Locate every blood parasite and identify its species.
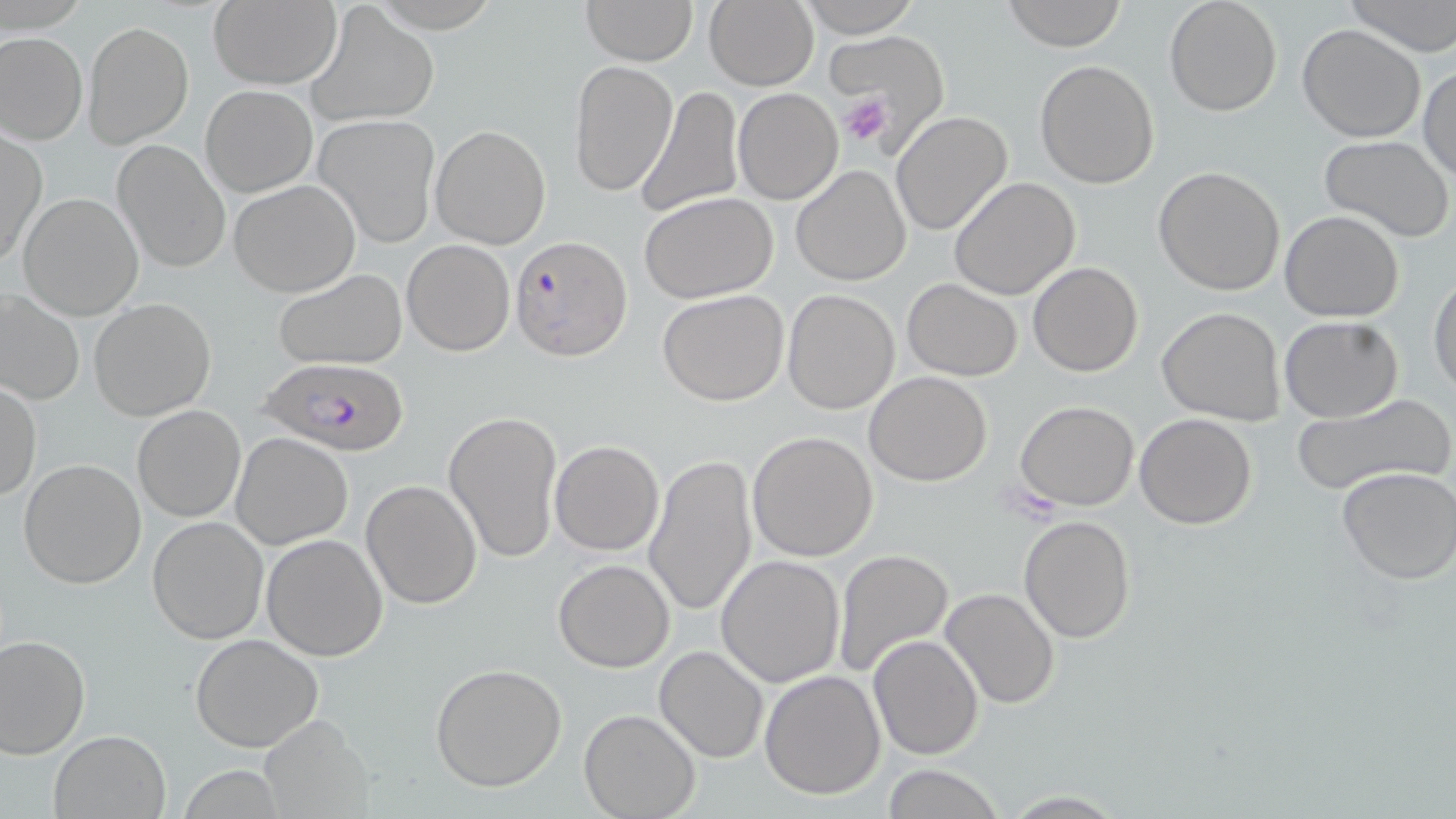
Approximate bounding boxes as [x1, y1, x2, y2] in pixels.
Plasmodium falciparum-infected red blood cells: [511, 236, 630, 358], [257, 358, 410, 454].
No Plasmodium ovale, Plasmodium malariae, Plasmodium vivax, Babesia divergens, or Trypanosoma brucei observed.

{
  "slide_level_diagnosis": "Plasmodium falciparum",
  "stain": "May-Grünwald-Giemsa",
  "platelet_locations": "approximate bounding boxes as [x1, y1, x2, y2] in pixels: [838, 92, 895, 146]",
  "image_size": "1456×819 pixels",
  "uninfected_red_blood_cell_locations": "approximate bounding boxes as [x1, y1, x2, y2] in pixels: [581, 0, 697, 65], [703, 0, 818, 91], [798, 0, 922, 39], [1002, 0, 1128, 51], [1164, 0, 1281, 116], [1343, 0, 1456, 56], [207, 1, 342, 89], [307, 6, 437, 126], [83, 22, 193, 148], [1296, 23, 1425, 142], [0, 31, 87, 145], [821, 31, 946, 132], [569, 59, 677, 196], [1034, 59, 1161, 189], [1418, 66, 1455, 183], [635, 81, 742, 217], [202, 85, 315, 197], [732, 88, 843, 204], [891, 111, 1013, 236], [314, 112, 441, 248], [429, 125, 552, 249], [1, 130, 45, 266], [1320, 134, 1454, 241], [111, 141, 230, 273], [791, 165, 910, 285], [1153, 166, 1285, 296], [947, 177, 1080, 301], [229, 180, 361, 297], [17, 192, 144, 320], [640, 192, 778, 304], [1280, 210, 1405, 323], [401, 240, 515, 355], [1028, 261, 1143, 377], [273, 268, 408, 371], [1430, 270, 1456, 401], [901, 278, 1022, 381], [1, 289, 83, 406], [782, 289, 900, 414], [657, 290, 789, 406], [87, 298, 217, 421], [1157, 308, 1286, 426], [1279, 316, 1403, 421], [865, 370, 992, 487], [1, 381, 41, 502], [1290, 395, 1456, 498], [1015, 400, 1139, 511], [132, 405, 246, 523], [444, 409, 564, 564], [1135, 413, 1257, 530], [748, 431, 879, 561], [230, 432, 354, 550], [550, 440, 663, 555], [645, 451, 758, 619], [18, 458, 147, 589], [1334, 465, 1456, 585], [360, 479, 484, 610], [148, 515, 268, 644], [1018, 515, 1137, 644], [260, 533, 388, 662], [832, 549, 954, 678], [715, 554, 845, 688], [552, 558, 675, 672], [941, 587, 1061, 710], [0, 634, 90, 757], [190, 634, 324, 752], [868, 635, 983, 759], [655, 646, 769, 762], [428, 663, 569, 792], [759, 669, 886, 799], [611, 672, 737, 797], [579, 710, 702, 819], [259, 717, 370, 815], [49, 730, 171, 818], [879, 765, 1006, 819], [998, 791, 1130, 818]",
  "preparation": "thin blood film",
  "magnification": "1000x",
  "modality": "light microscopy",
  "field_of_view": "one of a larger specimen"
}